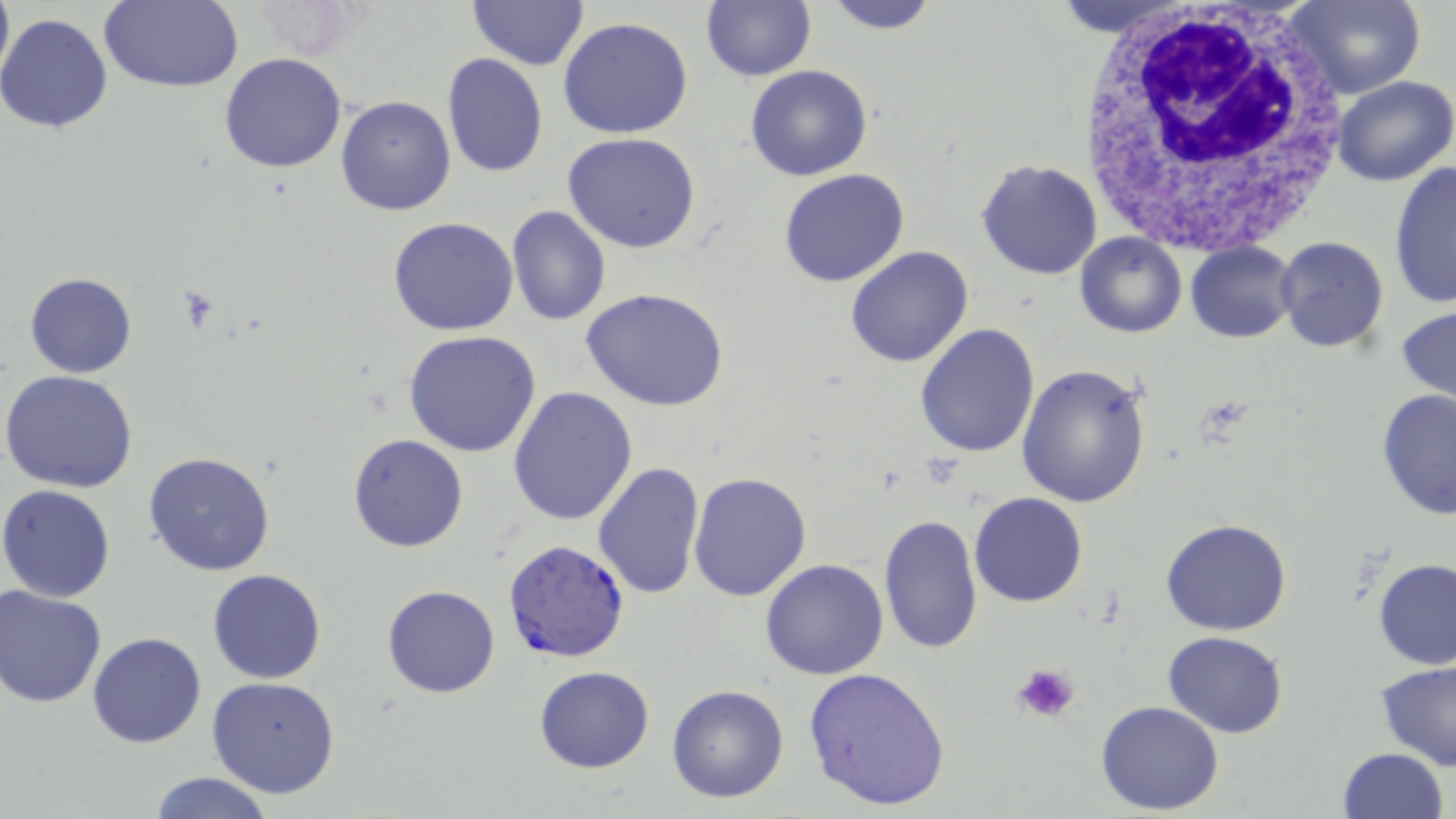 Approximate bounding boxes as (x1,y1)-(x2,y2) corner pairs in pixels. Platelet locations: (1012,662)-(1082,726). Plasmodium falciparum-infected red blood cell locations: (502,539)-(631,663). Uninfected red blood cell locations: (0,0)-(16,97), (468,0)-(588,70), (701,0)-(815,81), (817,0)-(942,35), (1054,0)-(1190,34), (1286,0)-(1426,101), (98,1)-(244,92), (0,13)-(116,133), (559,16)-(694,139), (219,53)-(347,174), (441,53)-(548,178), (746,65)-(873,182), (1331,74)-(1456,186), (335,96)-(456,217), (562,133)-(702,254), (977,158)-(1104,279), (1390,159)-(1455,308), (777,168)-(910,288), (506,206)-(612,327), (388,217)-(518,336), (1074,233)-(1186,339), (1274,235)-(1391,354), (1185,241)-(1300,343), (845,245)-(975,368), (24,272)-(137,377), (582,288)-(732,412), (1397,301)-(1456,415), (915,321)-(1040,456), (403,331)-(544,459), (1017,364)-(1152,508), (2,371)-(139,493), (508,385)-(640,526), (1377,389)-(1456,521), (348,433)-(469,551), (144,450)-(275,576), (593,462)-(706,599), (687,472)-(812,602), (1,484)-(118,602), (969,492)-(1088,607), (878,513)-(983,655), (1160,518)-(1293,636), (760,557)-(889,679), (1374,558)-(1456,670), (207,567)-(327,684), (0,585)-(107,708), (381,585)-(500,698), (1164,630)-(1288,738), (87,632)-(206,748), (1376,659)-(1456,770), (534,666)-(655,773), (803,668)-(950,811), (207,676)-(341,797), (666,683)-(791,803), (1095,700)-(1226,815), (1336,746)-(1450,819), (146,772)-(276,819). White blood cell locations: (1076,0)-(1357,255). Slide-level diagnosis: Plasmodium falciparum. May-Grünwald-Giemsa stain. Image is 1456×819 pixels. 1000x magnification. Light microscopy. One field of a larger specimen. Thin blood smear.